State which cell type is depicted.
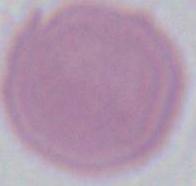
An erythrocyte.

1000x magnification. Micrograph.